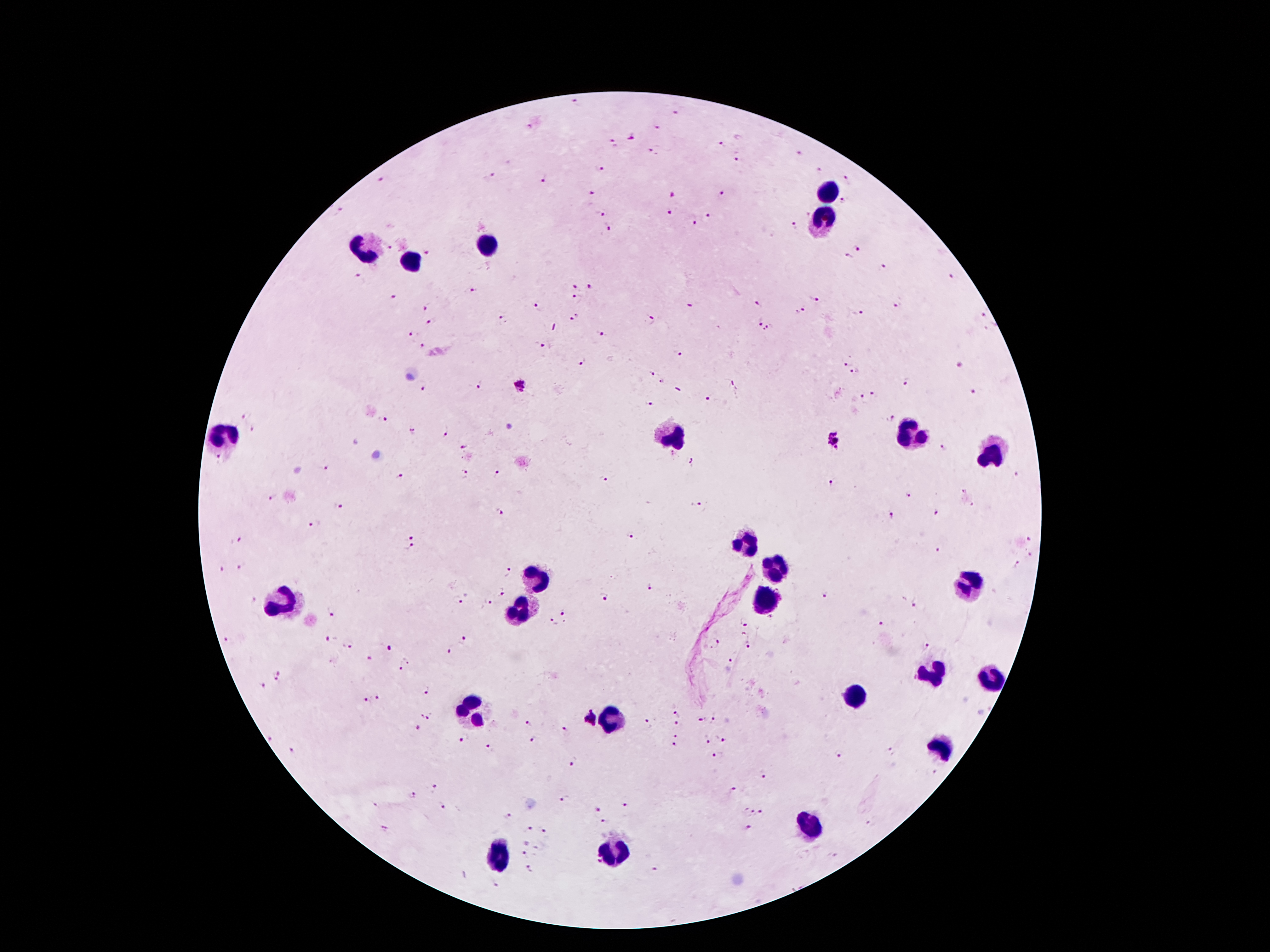 Image is 1270×952 pixels. 100x magnification. Giemsa-stained preparation. Thick blood smear. Patient malaria status: infected with Plasmodium falciparum. Single field of view. Smartphone photograph taken through the microscope eyepiece.